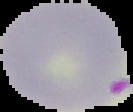

Summary:
  - Image size: 133×112 pixels
  - Preparation: thin blood smear
  - Malaria status: parasitized
  - Image type: segmented cell region on a black background